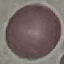

Result: negative for malaria parasites. Giemsa stain. Thin blood smear. Automatically extracted cell patch, resized to 64 × 64 pixels. Photographed with a smartphone camera at the microscope eyepiece.